Locate every blood parasite and identify its species.
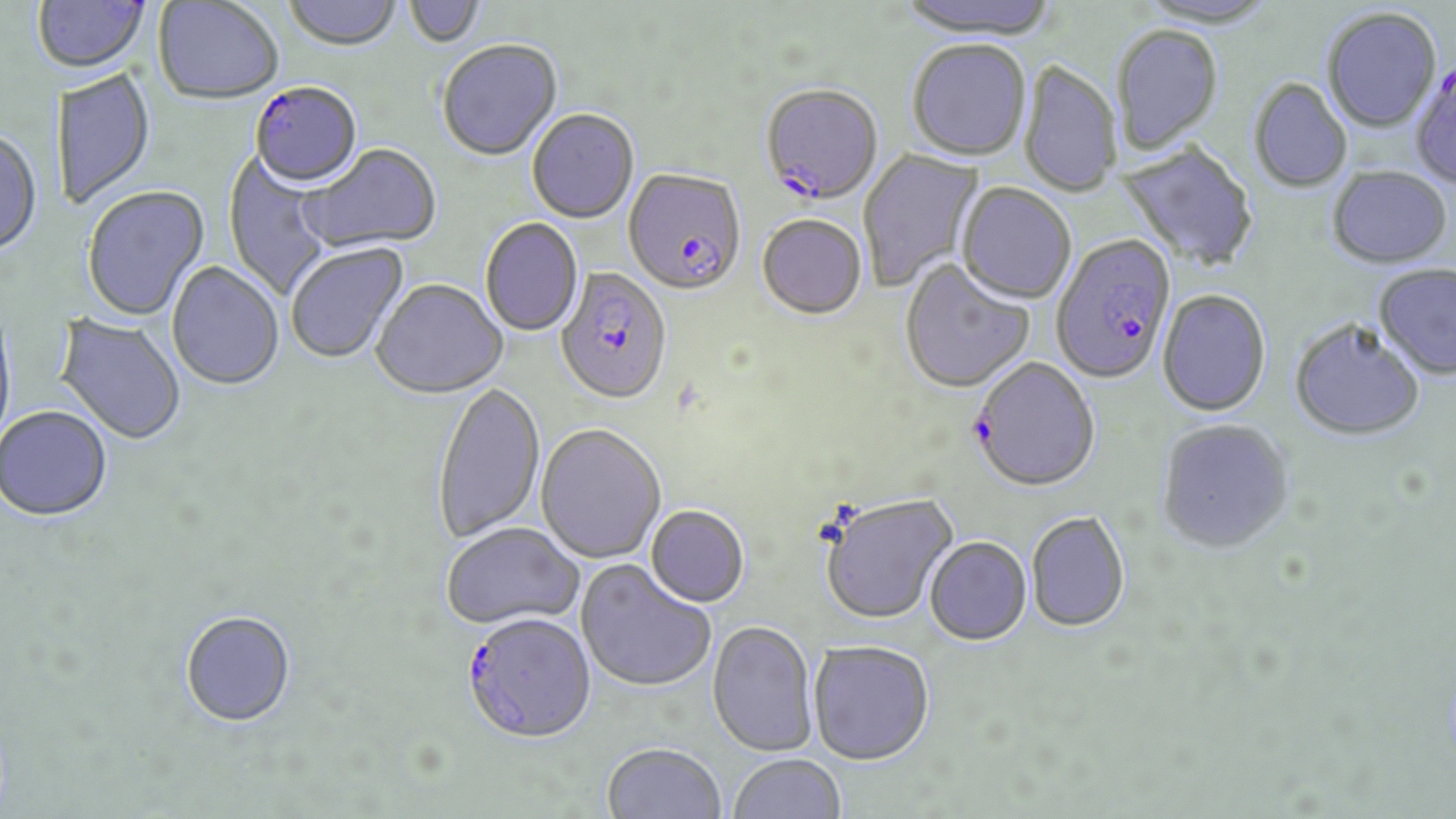
Approximate bounding boxes as (x1, y1, x2, y2) in pixels.
Plasmodium falciparum-infected red blood cells: (253, 80, 370, 187), (760, 86, 883, 207), (624, 168, 746, 296), (1051, 236, 1176, 384), (555, 268, 673, 405), (973, 358, 1100, 492), (462, 612, 596, 744).
No Plasmodium ovale, Plasmodium malariae, Plasmodium vivax, Babesia divergens, or Trypanosoma brucei observed.

Summary:
  - Uninfected red blood cell locations: (33, 0, 150, 73), (283, 0, 402, 51), (405, 0, 486, 48), (896, 0, 1060, 40), (153, 1, 283, 105), (1321, 9, 1442, 134), (1112, 26, 1224, 157), (437, 40, 563, 163), (907, 41, 1031, 162), (1410, 59, 1456, 192), (1017, 61, 1122, 198), (50, 68, 156, 209), (1247, 80, 1352, 194), (527, 109, 640, 224), (0, 127, 43, 258), (1116, 141, 1259, 273), (300, 144, 441, 255), (858, 148, 984, 292), (223, 151, 333, 301), (1327, 167, 1452, 270), (956, 183, 1076, 306), (81, 185, 211, 323), (757, 215, 867, 321), (480, 219, 584, 336), (286, 241, 410, 365), (900, 259, 1035, 394), (166, 261, 284, 391), (1374, 265, 1456, 382), (372, 280, 509, 401), (1157, 290, 1271, 417), (0, 309, 17, 452), (53, 312, 187, 446), (1289, 321, 1425, 443), (433, 382, 546, 544), (0, 407, 113, 524), (1157, 419, 1294, 555), (535, 424, 666, 564), (820, 493, 958, 625), (646, 505, 750, 607), (1026, 511, 1130, 633), (441, 522, 584, 630), (925, 537, 1032, 645), (576, 561, 715, 693), (180, 611, 297, 728), (707, 620, 819, 758), (808, 640, 935, 764), (601, 742, 726, 819), (728, 753, 846, 818)
  - Slide-level diagnosis: Plasmodium falciparum
  - Field of view: single
  - Preparation: thin blood film
  - Modality: light microscopy
  - Stain: May-Grünwald-Giemsa
  - Magnification: 1000x
  - Image size: 1456×819 pixels